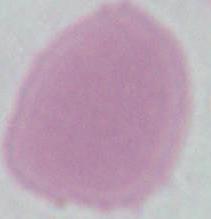
identification = erythrocyte
magnification = 1000x
modality = micrograph